Locate every Plasmodium malariae-infected red blood cell.
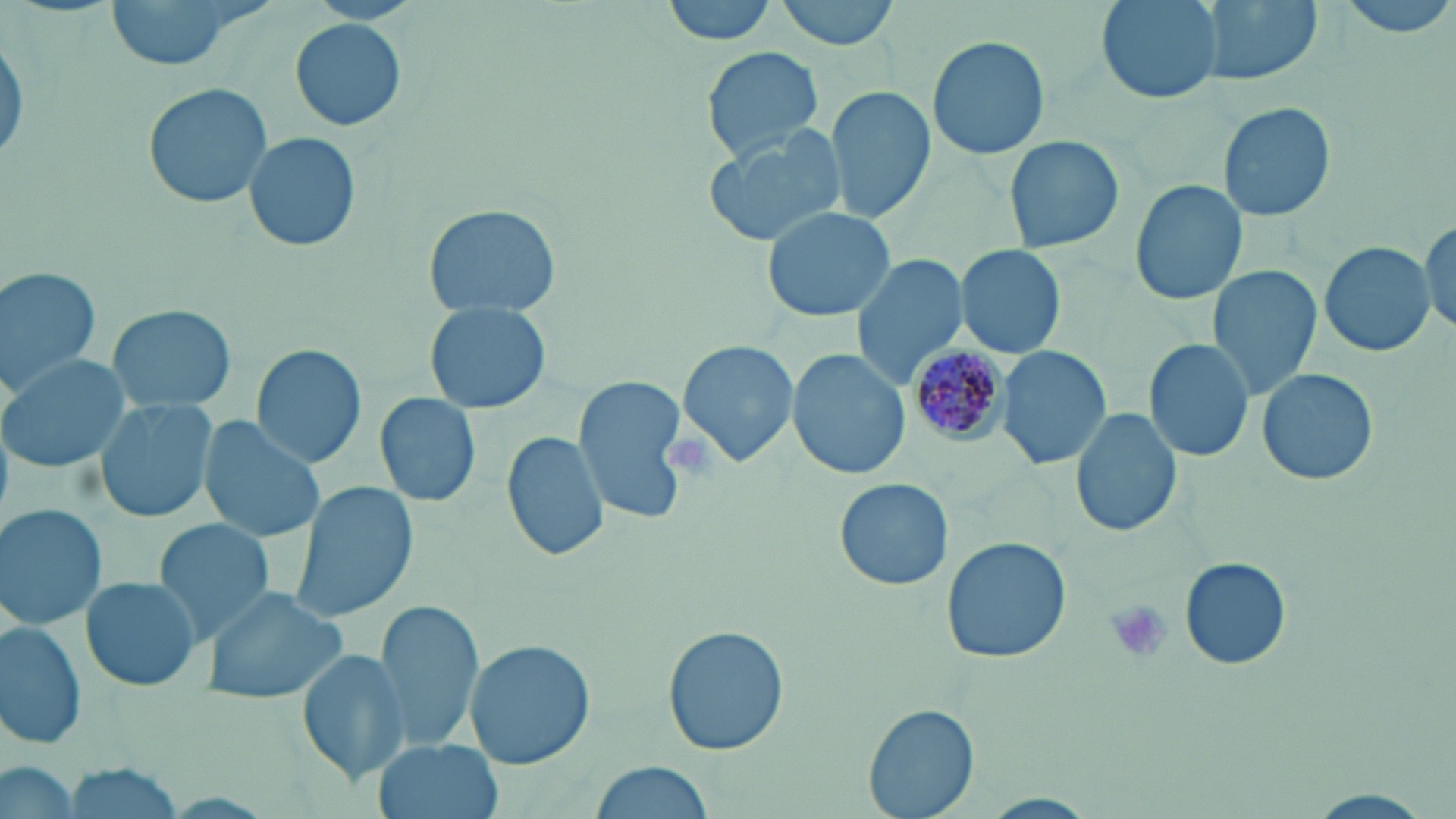

Approximate bounding boxes as [x1, y1, x2, y2] in pixels.
Plasmodium malariae-infected red blood cells: [906, 339, 1013, 448].

Uninfected red blood cell locations: [102, 0, 269, 72], [660, 0, 778, 46], [774, 0, 903, 50], [1097, 0, 1224, 104], [1198, 0, 1320, 86], [1332, 0, 1456, 37], [290, 18, 406, 130], [0, 33, 26, 168], [927, 34, 1052, 160], [700, 46, 824, 162], [142, 83, 273, 210], [828, 85, 935, 224], [1218, 102, 1337, 223], [701, 125, 847, 247], [243, 131, 362, 253], [1001, 135, 1125, 257], [1130, 178, 1247, 307], [423, 203, 561, 317], [759, 205, 898, 323], [1422, 217, 1456, 334], [1318, 241, 1432, 357], [955, 244, 1064, 358], [849, 254, 970, 390], [0, 265, 102, 394], [1208, 267, 1321, 399], [425, 302, 550, 417], [106, 304, 235, 415], [1143, 338, 1255, 463], [678, 340, 799, 468], [250, 345, 367, 468], [995, 346, 1111, 472], [787, 351, 909, 480], [0, 354, 136, 473], [1257, 367, 1380, 487], [572, 374, 689, 523], [374, 392, 481, 508], [95, 395, 218, 526], [1070, 407, 1182, 539], [197, 416, 325, 542], [501, 429, 611, 562], [834, 477, 953, 591], [289, 482, 418, 624], [0, 500, 107, 630], [152, 518, 275, 641], [943, 537, 1070, 664], [1179, 558, 1290, 671], [78, 575, 204, 693], [202, 585, 350, 705], [371, 600, 484, 752], [0, 617, 86, 751], [662, 625, 788, 756], [466, 640, 595, 769], [297, 646, 408, 783], [865, 702, 980, 818], [372, 738, 504, 819], [1, 758, 80, 819], [587, 761, 716, 816], [58, 764, 188, 815], [1296, 789, 1441, 819]. Platelet locations: [1105, 601, 1173, 665]. Slide-level diagnosis: Plasmodium malariae. Thin blood film. 1000x magnification. Optical microscopy. May-Grünwald-Giemsa stain. Single field of view. Image is 1456×819 pixels.